Give the extent of all uninfected red blood cells.
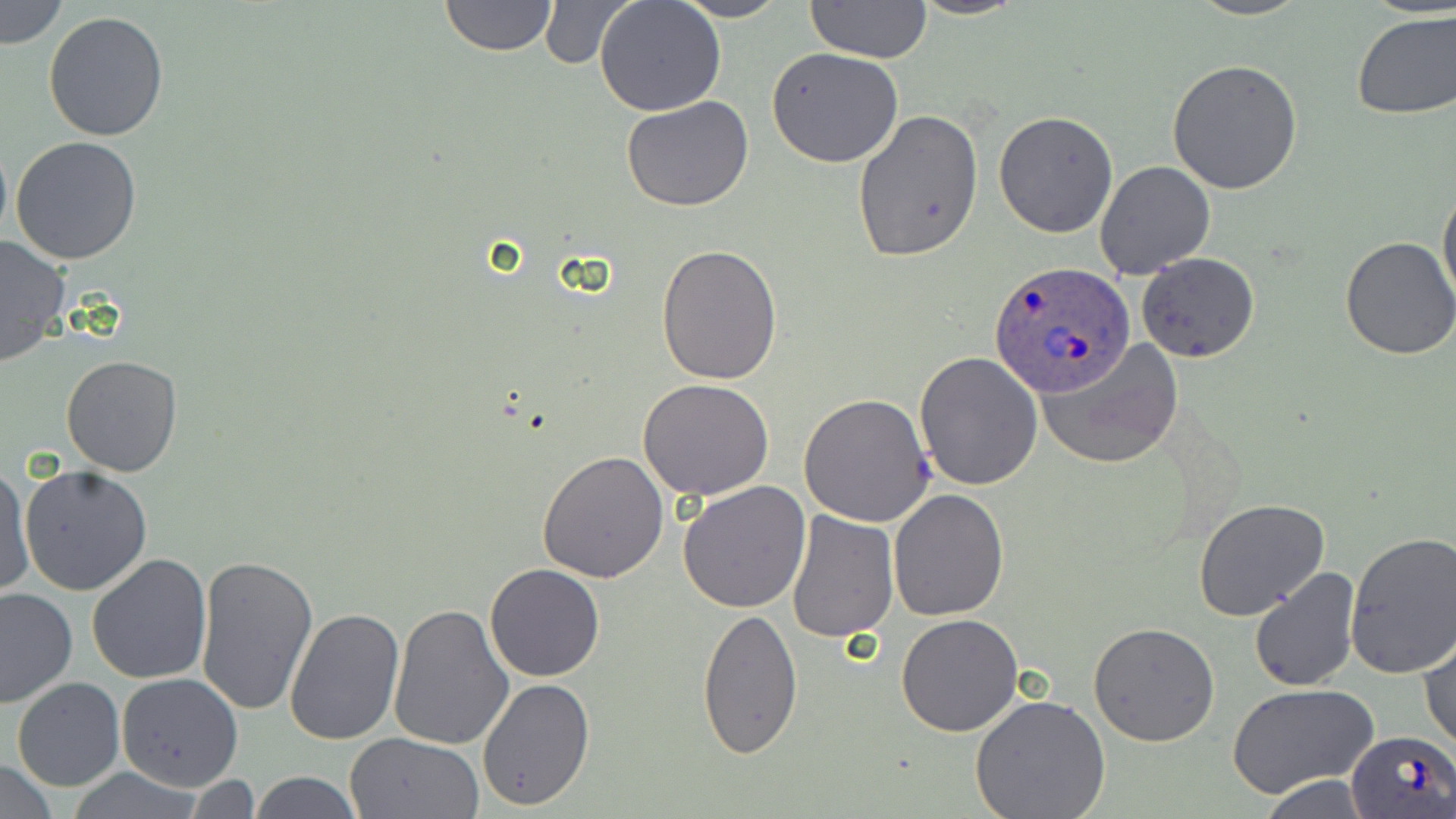
Approximate bounding boxes as named x1/y1/x2/y2 corners in pixels.
Uninfected red blood cells: (x1=2, y1=0, x2=68, y2=48), (x1=439, y1=0, x2=557, y2=57), (x1=672, y1=0, x2=790, y2=23), (x1=805, y1=0, x2=931, y2=65), (x1=908, y1=0, x2=1026, y2=20), (x1=1187, y1=0, x2=1310, y2=21), (x1=594, y1=1, x2=726, y2=117), (x1=535, y1=2, x2=633, y2=70), (x1=1351, y1=9, x2=1456, y2=120), (x1=42, y1=10, x2=169, y2=143), (x1=766, y1=47, x2=906, y2=168), (x1=1166, y1=59, x2=1303, y2=195), (x1=620, y1=95, x2=753, y2=212), (x1=852, y1=108, x2=984, y2=262), (x1=993, y1=111, x2=1118, y2=238), (x1=10, y1=136, x2=143, y2=265), (x1=1095, y1=160, x2=1216, y2=279), (x1=1438, y1=182, x2=1456, y2=308), (x1=0, y1=237, x2=71, y2=367), (x1=1339, y1=237, x2=1456, y2=359), (x1=656, y1=242, x2=783, y2=385), (x1=1136, y1=252, x2=1258, y2=364), (x1=1040, y1=342, x2=1179, y2=468), (x1=912, y1=350, x2=1043, y2=491), (x1=61, y1=354, x2=183, y2=477), (x1=637, y1=380, x2=774, y2=501), (x1=798, y1=391, x2=935, y2=527), (x1=536, y1=448, x2=669, y2=582), (x1=1, y1=462, x2=34, y2=599), (x1=20, y1=465, x2=152, y2=597), (x1=677, y1=480, x2=811, y2=613), (x1=887, y1=488, x2=1008, y2=623), (x1=1193, y1=499, x2=1331, y2=621), (x1=786, y1=511, x2=900, y2=644), (x1=1342, y1=528, x2=1456, y2=678), (x1=194, y1=551, x2=320, y2=719), (x1=86, y1=553, x2=214, y2=685), (x1=483, y1=564, x2=605, y2=683), (x1=1247, y1=566, x2=1361, y2=693), (x1=1, y1=587, x2=76, y2=709), (x1=388, y1=603, x2=513, y2=750), (x1=284, y1=606, x2=406, y2=745), (x1=697, y1=608, x2=803, y2=759), (x1=896, y1=612, x2=1023, y2=737), (x1=1088, y1=623, x2=1220, y2=746), (x1=1419, y1=626, x2=1455, y2=753), (x1=115, y1=674, x2=243, y2=792), (x1=11, y1=677, x2=126, y2=791), (x1=478, y1=677, x2=595, y2=811), (x1=1226, y1=683, x2=1378, y2=800), (x1=969, y1=693, x2=1112, y2=819), (x1=344, y1=732, x2=484, y2=818), (x1=0, y1=759, x2=60, y2=817), (x1=249, y1=772, x2=363, y2=817), (x1=1253, y1=775, x2=1382, y2=817), (x1=185, y1=777, x2=267, y2=815).

slide-level diagnosis = Plasmodium ovale
magnification = 1000x
stain = May-Grünwald-Giemsa
image size = 1456×819 pixels
preparation = thin blood film
Plasmodium ovale-infected red blood cell locations = approximate bounding boxes as named x1/y1/x2/y2 corners in pixels: (x1=989, y1=260, x2=1135, y2=400), (x1=1346, y1=728, x2=1455, y2=816)
modality = light microscopy
field of view = one of a larger specimen